Name the parasite shown.
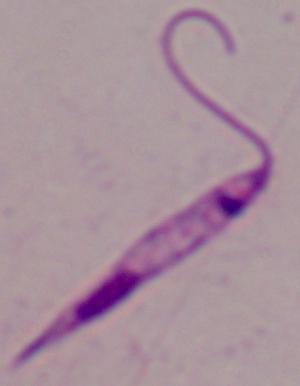
This is Leishmania.

1000x magnification. Micrograph.